Give the extent of all Plasmodium vivax-infected red blood cells.
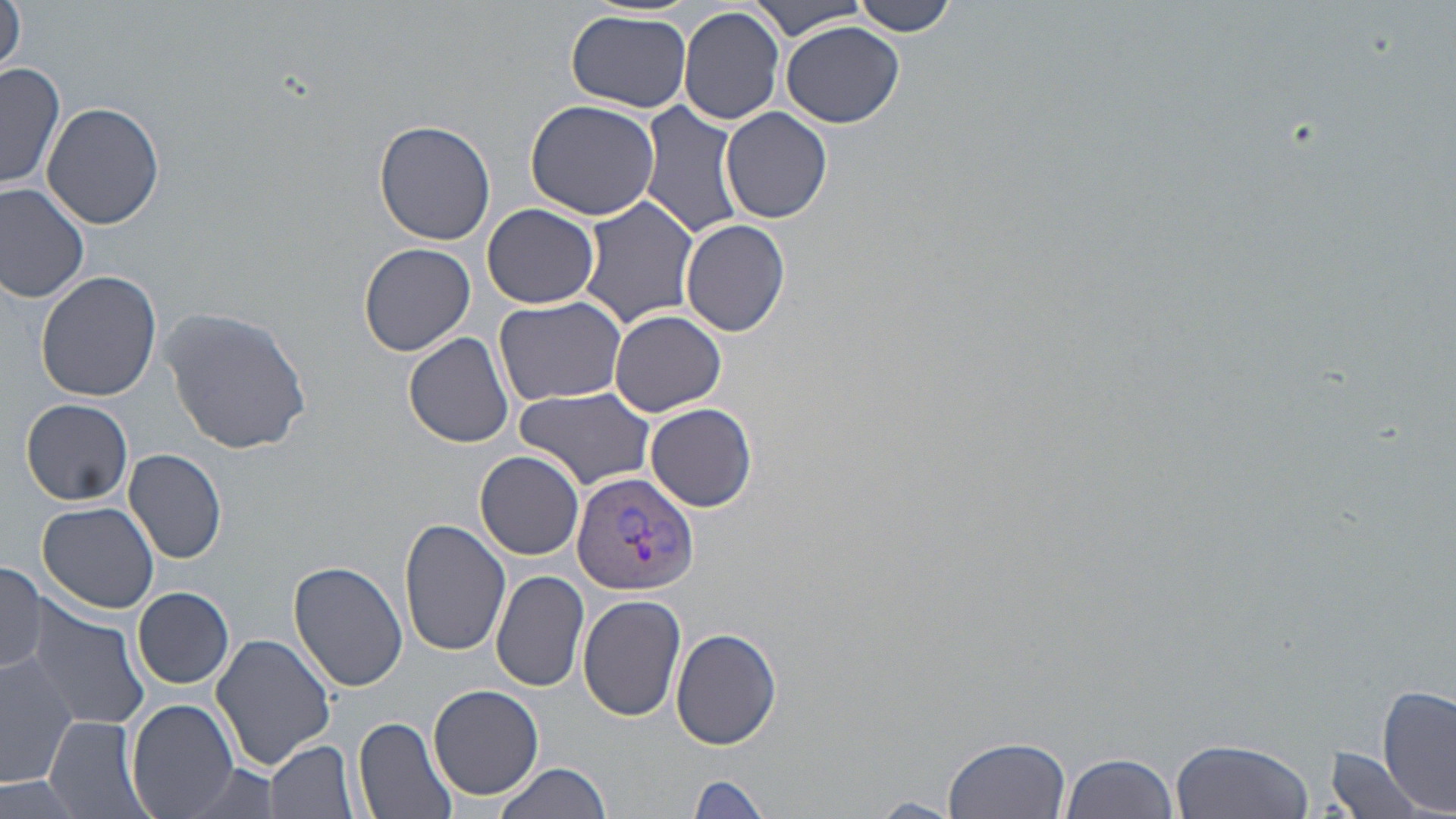

Approximate bounding boxes as [x1, y1, x2, y2] in pixels.
Plasmodium vivax-infected red blood cells: [572, 469, 699, 596].

Uninfected red blood cell locations: [749, 0, 868, 41], [848, 0, 958, 36], [0, 1, 27, 79], [678, 5, 786, 127], [567, 11, 693, 112], [782, 19, 905, 128], [0, 62, 64, 191], [524, 98, 661, 221], [43, 101, 164, 230], [639, 102, 747, 242], [721, 107, 832, 222], [703, 118, 813, 302], [372, 119, 498, 247], [0, 182, 90, 303], [579, 196, 699, 328], [482, 203, 600, 309], [681, 217, 790, 338], [360, 243, 476, 356], [37, 271, 162, 400], [494, 295, 626, 407], [159, 305, 312, 456], [610, 309, 727, 416], [403, 331, 515, 449], [516, 387, 657, 489], [21, 398, 134, 506], [644, 402, 757, 511], [124, 448, 227, 564], [475, 451, 586, 560], [38, 503, 161, 614], [399, 519, 511, 657], [0, 560, 47, 676], [289, 560, 409, 692], [491, 568, 590, 692], [133, 587, 236, 689], [578, 594, 685, 721], [19, 601, 150, 732], [670, 627, 782, 751], [212, 634, 337, 768], [1, 649, 77, 789], [1377, 685, 1456, 812], [429, 686, 543, 799], [126, 699, 241, 819], [48, 715, 153, 819], [353, 715, 458, 819], [944, 735, 1072, 818], [1170, 738, 1315, 819], [266, 740, 360, 819], [1324, 748, 1432, 819], [1060, 751, 1179, 819], [494, 760, 615, 818], [172, 761, 285, 819], [3, 773, 86, 819], [686, 773, 775, 818], [866, 797, 962, 817]. Slide-level diagnosis: Plasmodium vivax. Captured at 1000x magnification. Image is 1456×819 pixels. May-Grünwald-Giemsa-stained preparation. Light microscopy. Single field of view. Thin blood film.